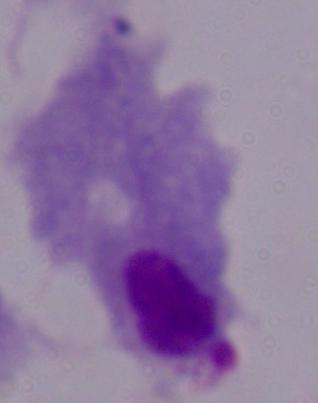
{
  "identification": "trichomonad",
  "modality": "micrograph",
  "magnification": "1000x"
}